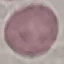 Result: negative for malaria parasites. Photographed with a smartphone camera at the microscope eyepiece. Thin blood smear. Giemsa-stained preparation. Cell patch, automatically extracted from a larger field of view and resized to 64 × 64 pixels.